Assess the morphology of the red blood cells.
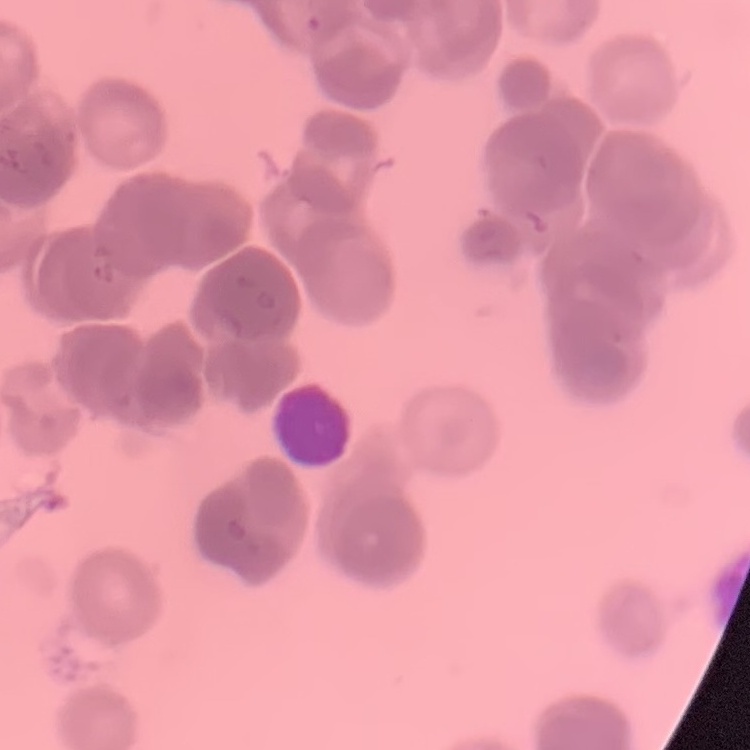
Rouleaux formation.

Thin peripheral smear. Field's or Giemsa stain. One tile cut from a larger photomicrograph.